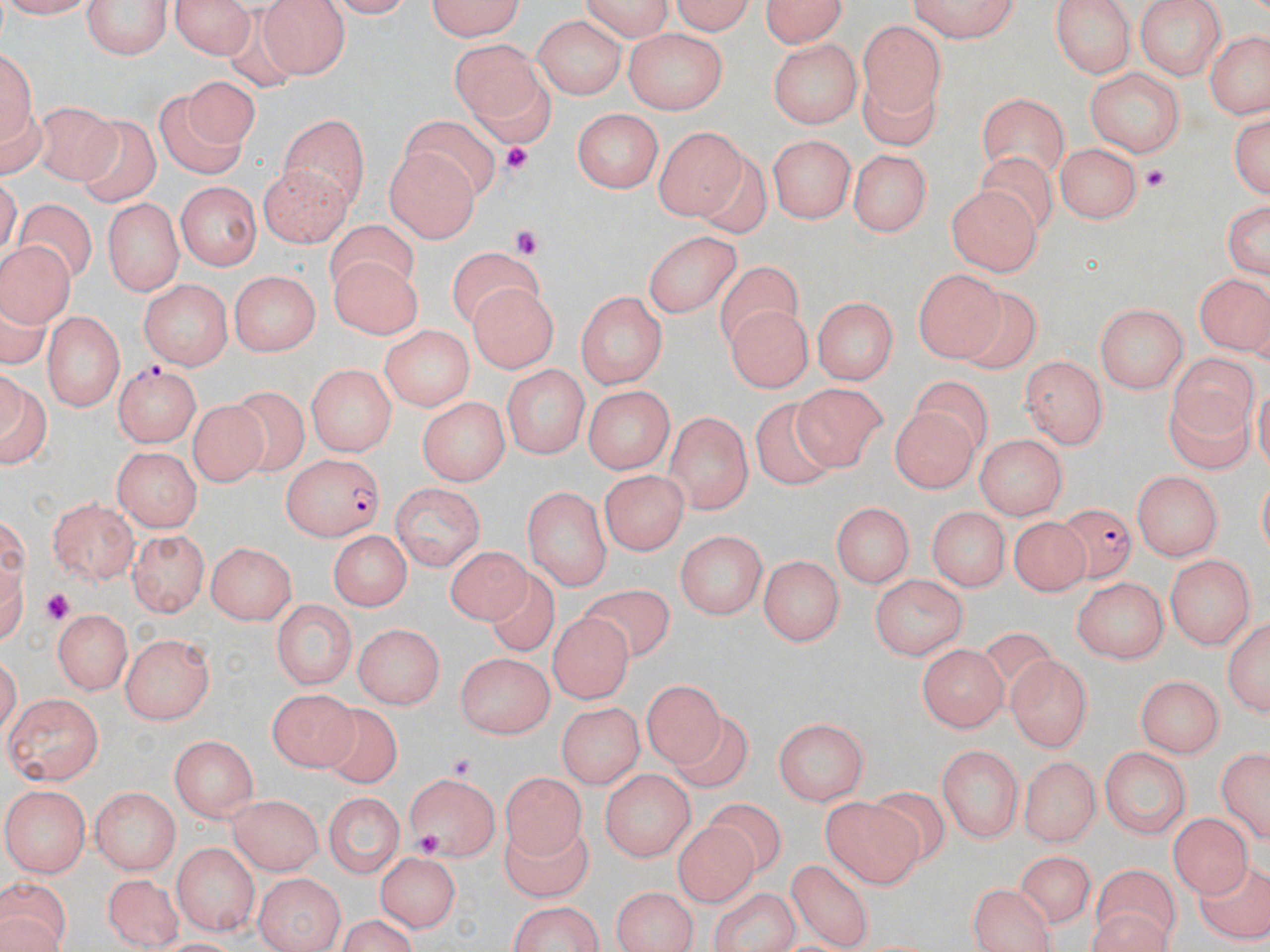

Approximate bounding boxes as (x1, y1, x2, y2) in pixels. Uninfected red blood cell locations: (0, 0, 91, 18), (84, 0, 175, 60), (166, 0, 260, 58), (424, 0, 531, 41), (574, 0, 675, 38), (670, 0, 760, 35), (757, 0, 852, 48), (1135, 0, 1226, 79), (905, 1, 1027, 43), (260, 2, 347, 77), (1050, 2, 1136, 81), (532, 16, 625, 100), (857, 19, 943, 120), (1205, 28, 1270, 121), (623, 31, 725, 111), (449, 38, 550, 133), (767, 38, 863, 126), (0, 42, 36, 162), (1084, 65, 1187, 155), (184, 79, 261, 151), (859, 80, 948, 148), (153, 89, 242, 177), (977, 93, 1068, 177), (38, 98, 113, 184), (1227, 106, 1269, 197), (572, 107, 664, 194), (279, 110, 371, 209), (81, 111, 158, 209), (400, 112, 498, 200), (654, 127, 750, 225), (769, 134, 856, 225), (1057, 142, 1144, 222), (384, 145, 478, 243), (848, 147, 932, 235), (257, 164, 353, 247), (172, 181, 260, 270), (947, 184, 1037, 276), (14, 196, 97, 282), (1223, 198, 1269, 282), (104, 202, 182, 293), (325, 222, 417, 291), (641, 226, 743, 320), (1, 239, 75, 336), (328, 250, 419, 339), (449, 251, 548, 324), (719, 261, 807, 344), (913, 268, 1003, 362), (231, 269, 322, 356), (1195, 270, 1268, 358), (139, 278, 231, 368), (469, 283, 558, 375), (947, 290, 1044, 373), (572, 291, 666, 391), (815, 294, 900, 382), (728, 302, 810, 394), (1096, 302, 1189, 390), (43, 308, 125, 414), (381, 327, 474, 413), (1167, 354, 1260, 431), (1021, 355, 1109, 450), (305, 361, 397, 457), (502, 365, 590, 458), (0, 370, 48, 470), (792, 380, 889, 468), (581, 384, 678, 471), (233, 386, 312, 478), (1167, 390, 1255, 473), (418, 395, 511, 484), (748, 396, 836, 491), (188, 398, 278, 482), (890, 398, 985, 494), (665, 410, 752, 512), (976, 431, 1068, 521), (111, 447, 199, 534), (599, 468, 686, 558), (1131, 469, 1223, 560), (521, 481, 612, 587), (389, 482, 486, 565), (48, 498, 139, 586), (835, 500, 915, 588), (931, 505, 1006, 592), (1013, 515, 1089, 595), (128, 528, 208, 616), (326, 529, 412, 610), (673, 529, 767, 617), (206, 540, 297, 625), (446, 544, 532, 624), (759, 554, 845, 646), (1166, 554, 1257, 651), (488, 566, 557, 655), (869, 573, 969, 658), (1070, 577, 1167, 664), (577, 579, 677, 663), (272, 598, 354, 692), (542, 607, 632, 705), (52, 611, 129, 693), (1224, 612, 1267, 717), (355, 622, 445, 707), (121, 635, 214, 724), (916, 645, 1004, 733), (455, 650, 556, 737), (1005, 655, 1092, 750), (642, 674, 725, 768), (1133, 674, 1225, 756), (271, 686, 355, 771), (4, 694, 103, 788), (555, 702, 641, 788), (315, 704, 404, 788), (772, 712, 870, 803), (671, 715, 754, 787), (167, 734, 261, 820), (1217, 742, 1268, 841), (937, 743, 1024, 843), (1102, 747, 1191, 840), (1022, 755, 1096, 849), (598, 768, 693, 862), (402, 770, 499, 862), (499, 773, 594, 862), (870, 780, 953, 866), (5, 785, 90, 878), (89, 787, 181, 875), (228, 793, 320, 872), (328, 795, 400, 879), (701, 795, 790, 875), (822, 797, 920, 888), (1170, 815, 1258, 903), (504, 820, 594, 900), (669, 821, 758, 904), (169, 843, 257, 934), (1017, 847, 1100, 928), (375, 851, 462, 930), (1194, 859, 1270, 940), (785, 861, 879, 947), (1093, 863, 1180, 933), (103, 871, 185, 948), (255, 874, 343, 952), (0, 877, 72, 951), (967, 880, 1059, 952), (608, 886, 695, 950), (712, 888, 801, 949), (501, 899, 609, 952), (1087, 909, 1174, 952), (330, 916, 421, 950). Platelet locations: (499, 140, 533, 176), (1142, 164, 1168, 192), (507, 224, 544, 260), (36, 589, 72, 624), (447, 752, 480, 780), (413, 831, 445, 859). Plasmodium falciparum-infected red blood cell locations: (113, 360, 200, 447), (280, 453, 387, 541), (1053, 502, 1144, 586). Slide-level diagnosis: Plasmodium falciparum. Light microscopy. One field of a larger specimen. 1000x magnification. Image is 1270×952 pixels. Thin blood film. May-Grünwald-Giemsa stain.